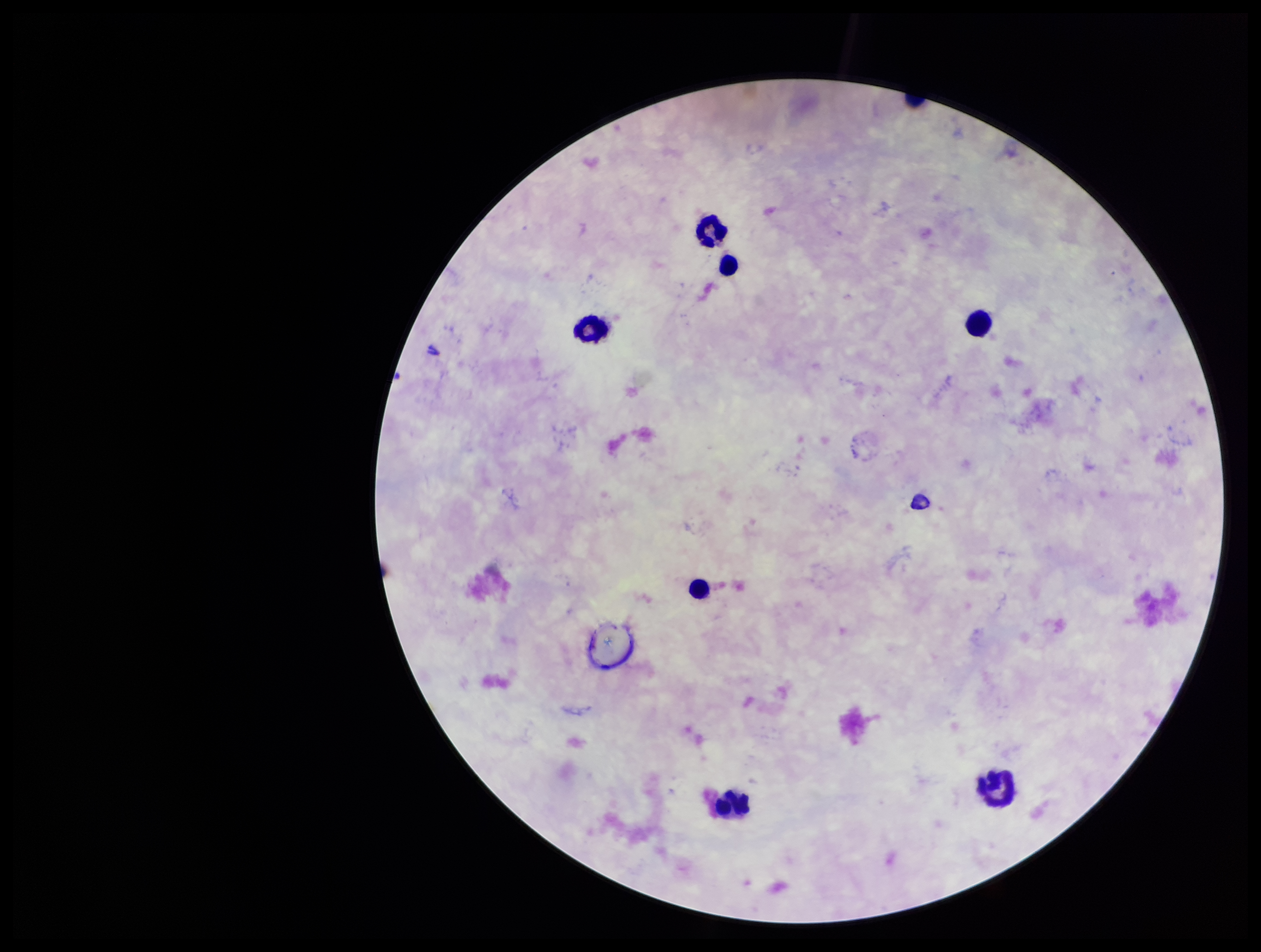

Summary:
  - Patient malaria status: negative
  - Stain: Giemsa
  - Plasmodium parasites: none seen
  - Field of view: single
  - Capture: smartphone photograph through the microscope eyepiece
  - Image size: 1261×952 pixels
  - Leukocyte count: 7
  - Preparation: thick blood smear
  - Parasite count: 0